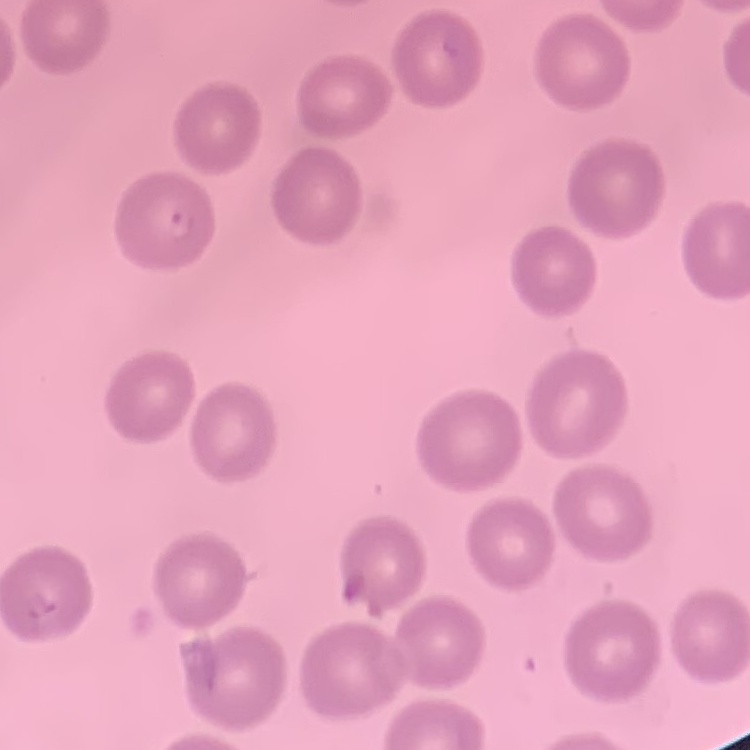

Summary:
  - Red blood cell morphology: no rouleaux formation
  - Preparation: thin blood film
  - Image type: square crop of a larger photomicrograph
  - Stain: Field's or Giemsa